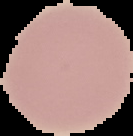

Summary:
  - Preparation: thin blood film
  - Malaria status: uninfected
  - Image type: segmented cell region on a black background
  - Image size: 133×136 pixels